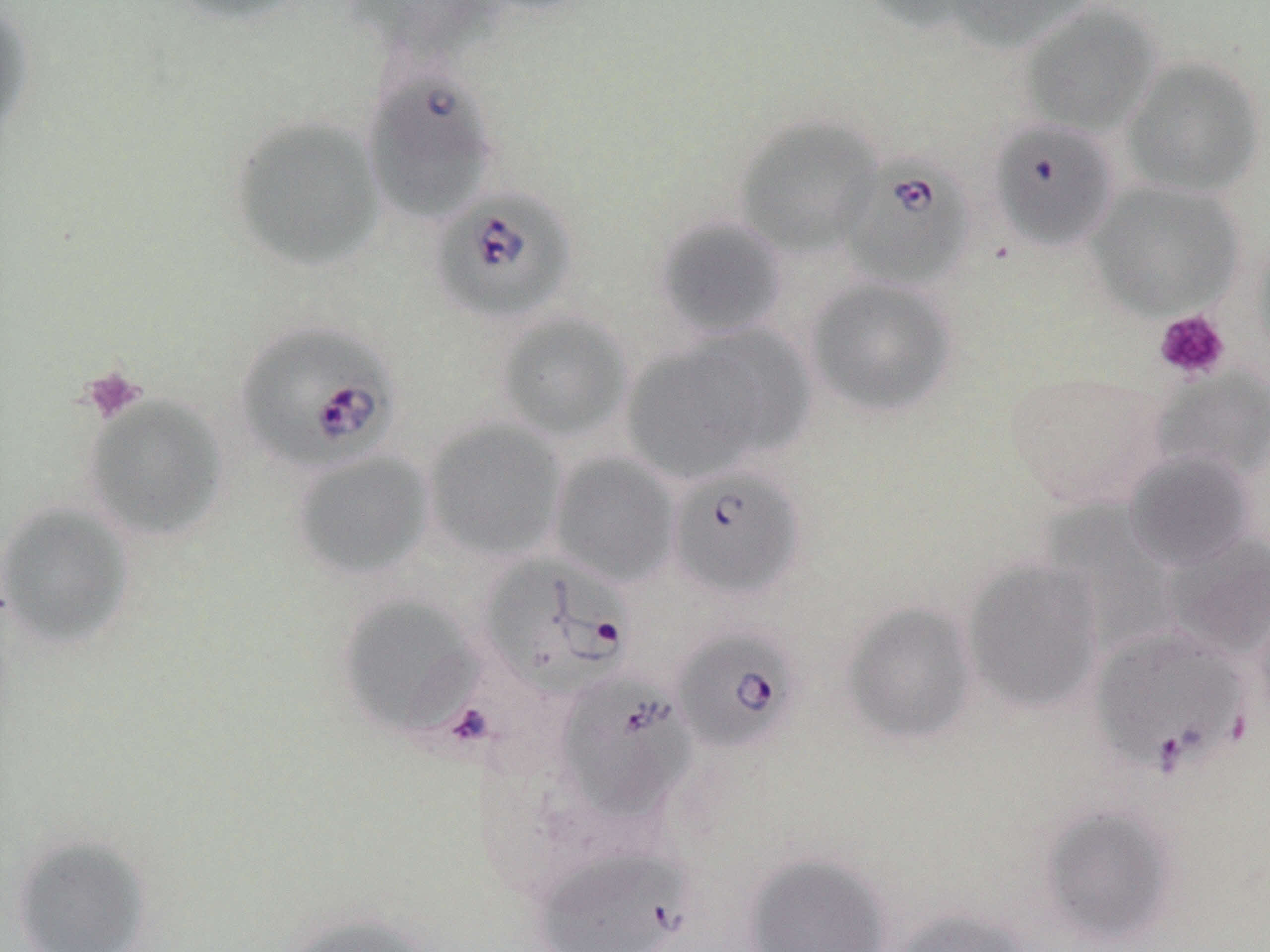
slide-level diagnosis = Babesia divergens
preparation = thin blood film
modality = optical microscopy
platelet locations = approximate bounding boxes as [x1, y1, x2, y2] in pixels: [1153, 309, 1230, 382], [80, 366, 147, 425]
Babesia divergens-infected red blood cell locations = approximate bounding boxes as [x1, y1, x2, y2] in pixels: [988, 119, 1119, 252], [839, 155, 976, 290], [430, 186, 578, 325], [235, 320, 401, 473], [668, 465, 804, 600], [478, 553, 636, 703], [1089, 625, 1251, 776], [671, 627, 801, 752], [553, 670, 697, 823], [532, 845, 696, 952]
stain = May-Grünwald-Giemsa
image size = 1270×952 pixels
field of view = one of a larger specimen
uninfected red blood cell locations = approximate bounding boxes as [x1, y1, x2, y2] in pixels: [162, 0, 311, 26], [344, 0, 507, 66], [861, 0, 992, 34], [946, 0, 1098, 53], [0, 3, 35, 142], [1018, 3, 1162, 137], [1121, 56, 1265, 198], [366, 70, 498, 225], [733, 114, 883, 257], [227, 115, 386, 272], [1086, 181, 1245, 319], [652, 213, 789, 341], [1250, 231, 1270, 368], [805, 277, 958, 418], [494, 311, 633, 442], [621, 329, 805, 485], [1148, 366, 1270, 481], [1005, 370, 1167, 510], [83, 394, 228, 542], [423, 419, 566, 562], [291, 451, 434, 580], [1125, 451, 1257, 572], [548, 452, 680, 587], [1, 503, 134, 648], [1162, 532, 1270, 660], [961, 558, 1105, 714], [1251, 589, 1270, 732], [336, 594, 482, 740], [842, 601, 980, 746], [1039, 804, 1179, 946], [11, 834, 153, 951], [742, 852, 893, 951], [890, 906, 1032, 952], [282, 911, 434, 952]
magnification = 1000x